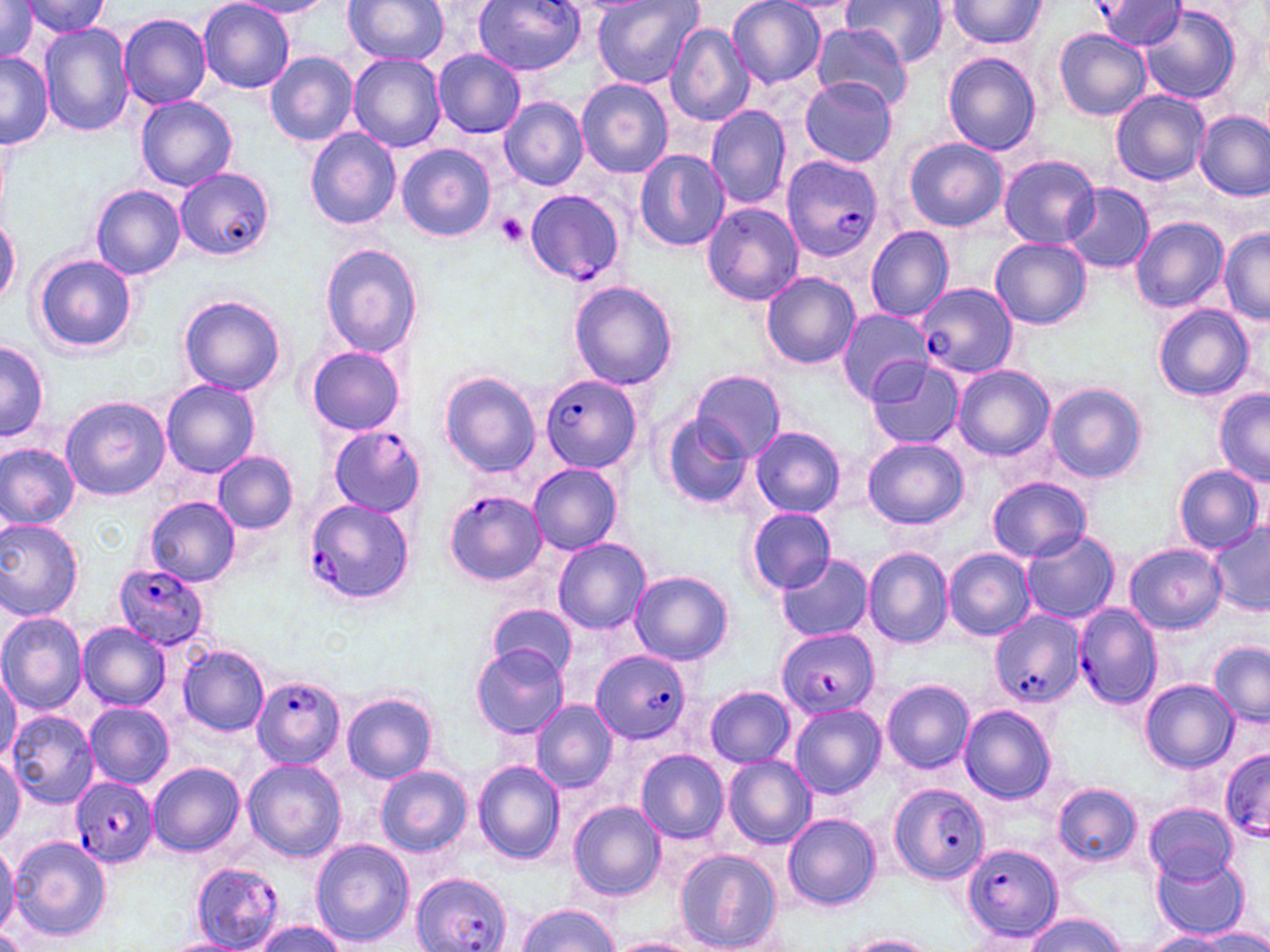
slide-level diagnosis = Plasmodium falciparum
magnification = 1000x
field of view = one of a larger specimen
stain = May-Grünwald-Giemsa
modality = optical microscopy
platelet locations = approximate bounding boxes as (x1,y1)-(x2,y2) corner pairs in pixels: (495,214)-(528,248)
Plasmodium falciparum-infected red blood cell locations = approximate bounding boxes as (x1,y1)-(x2,y2) corner pairs in pixels: (476,0)-(583,74), (1094,2)-(1187,49), (780,155)-(885,264), (174,167)-(275,262), (524,188)-(624,285), (917,282)-(1018,380), (541,374)-(643,473), (327,425)-(421,516), (444,492)-(544,586), (302,496)-(415,605), (112,564)-(211,650), (1074,602)-(1163,710), (989,610)-(1083,708), (775,629)-(878,719), (591,650)-(692,745), (251,675)-(345,770), (1221,750)-(1270,840), (69,778)-(158,869), (889,784)-(990,885), (961,843)-(1063,944), (192,862)-(284,949), (410,870)-(514,952)
preparation = thin blood smear
image size = 1270×952 pixels
uninfected red blood cell locations = approximate bounding boxes as (x1,y1)-(x2,y2) corner pairs in pixels: (344,0)-(448,65), (591,0)-(701,88), (728,0)-(825,87), (844,0)-(950,67), (0,1)-(41,62), (199,1)-(294,92), (231,1)-(334,17), (774,1)-(861,15), (944,1)-(1050,50), (25,2)-(112,39), (1138,5)-(1240,104), (118,11)-(211,110), (665,22)-(753,127), (38,23)-(134,136), (808,23)-(913,111), (1054,28)-(1151,120), (433,48)-(527,137), (265,51)-(358,147), (0,52)-(52,149), (943,53)-(1043,155), (348,54)-(447,151), (335,77)-(433,211), (576,78)-(673,178), (798,78)-(898,166), (1110,89)-(1211,186), (135,95)-(238,191), (499,97)-(588,190), (705,106)-(791,210), (1195,110)-(1269,199), (305,129)-(402,230), (904,137)-(1007,231), (396,142)-(497,242), (633,148)-(729,251), (998,153)-(1100,247), (1061,183)-(1154,274), (90,185)-(185,278), (701,202)-(803,306), (1130,215)-(1228,312), (1,216)-(21,310), (865,226)-(954,322), (1217,230)-(1270,323), (989,238)-(1093,329), (320,244)-(421,357), (33,253)-(137,355), (760,271)-(861,370), (569,281)-(679,390), (178,295)-(286,394), (1152,301)-(1256,402), (836,308)-(934,404), (1,339)-(48,445), (302,345)-(407,436), (864,358)-(964,450), (951,365)-(1056,462), (439,369)-(540,476), (691,371)-(783,462), (161,380)-(261,477), (1044,381)-(1148,483), (1216,388)-(1270,484), (60,395)-(170,501), (661,412)-(758,511), (751,426)-(846,517), (863,437)-(968,530), (0,440)-(81,530), (214,452)-(298,533), (529,462)-(623,556), (1172,465)-(1263,553), (989,476)-(1092,562), (144,496)-(241,587), (747,507)-(838,594), (0,518)-(84,620), (1208,522)-(1269,613), (1020,529)-(1120,626), (553,538)-(650,634), (1125,542)-(1226,635), (943,548)-(1036,641), (863,549)-(953,647), (773,554)-(872,641), (630,570)-(733,665), (489,603)-(579,679), (0,610)-(87,713), (77,623)-(170,709), (1209,642)-(1269,725), (471,644)-(569,739), (179,645)-(269,737), (0,667)-(20,766), (881,680)-(974,774), (1140,681)-(1237,772), (703,686)-(797,768), (342,692)-(438,783), (531,700)-(617,792), (85,702)-(174,789), (789,703)-(886,798), (959,704)-(1057,804), (6,710)-(100,809), (636,749)-(729,845), (0,754)-(24,847), (722,755)-(816,849), (242,759)-(345,864), (148,761)-(245,858), (472,761)-(566,864), (375,765)-(472,857), (1052,782)-(1144,868), (568,801)-(666,899), (1144,802)-(1236,883), (783,813)-(882,911), (8,835)-(110,941), (311,840)-(414,946), (0,844)-(19,938), (672,848)-(783,951), (1152,856)-(1247,939), (516,902)-(619,952), (1025,914)-(1125,952), (251,920)-(346,952), (1193,929)-(1270,951), (1144,931)-(1229,952), (842,935)-(934,951), (160,936)-(252,952), (610,936)-(698,952)